Locate every blood parasite and identify its species.
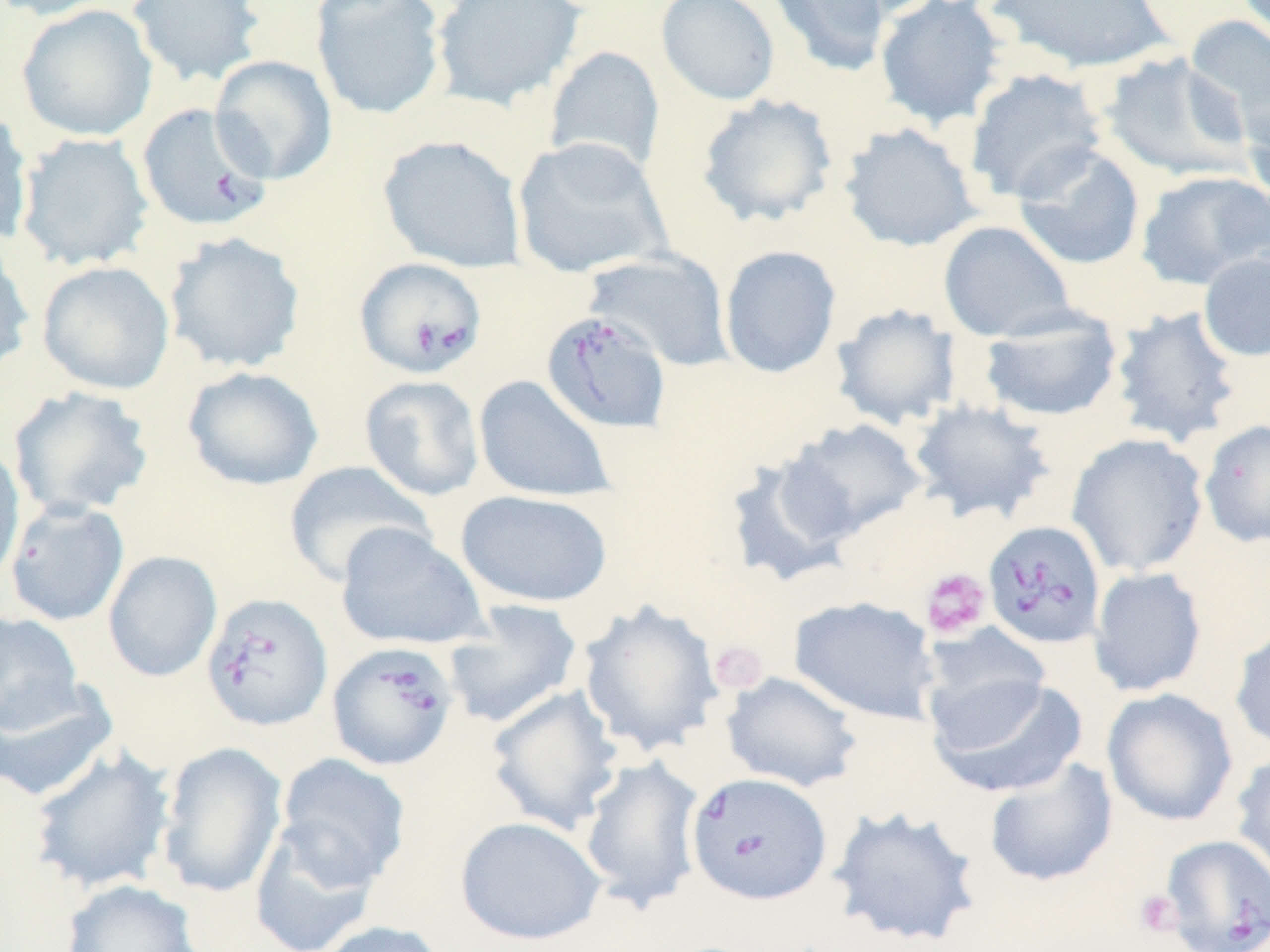

Approximate bounding boxes as named x1/y1/x2/y2 corners in pixels.
Babesia divergens-infected red blood cells: (x1=137, y1=102, x2=273, y2=232), (x1=354, y1=256, x2=488, y2=380), (x1=541, y1=310, x2=673, y2=435), (x1=983, y1=520, x2=1106, y2=649), (x1=199, y1=592, x2=333, y2=732), (x1=326, y1=640, x2=459, y2=771), (x1=686, y1=772, x2=832, y2=905), (x1=1158, y1=834, x2=1270, y2=951).
No Plasmodium falciparum, Plasmodium ovale, Plasmodium malariae, Plasmodium vivax, or Trypanosoma brucei observed.

Platelet locations: (x1=920, y1=567, x2=991, y2=640), (x1=709, y1=640, x2=769, y2=694), (x1=1134, y1=889, x2=1183, y2=937). Uninfected red blood cell locations: (x1=0, y1=0, x2=117, y2=20), (x1=126, y1=0, x2=265, y2=87), (x1=310, y1=0, x2=447, y2=120), (x1=431, y1=0, x2=586, y2=111), (x1=655, y1=0, x2=781, y2=106), (x1=766, y1=0, x2=892, y2=78), (x1=819, y1=0, x2=945, y2=20), (x1=875, y1=0, x2=1009, y2=130), (x1=989, y1=0, x2=1172, y2=73), (x1=16, y1=4, x2=158, y2=141), (x1=1184, y1=15, x2=1270, y2=147), (x1=544, y1=45, x2=666, y2=177), (x1=1099, y1=51, x2=1254, y2=183), (x1=209, y1=55, x2=338, y2=185), (x1=964, y1=68, x2=1109, y2=205), (x1=695, y1=93, x2=839, y2=228), (x1=1240, y1=93, x2=1270, y2=212), (x1=0, y1=107, x2=34, y2=247), (x1=838, y1=122, x2=983, y2=252), (x1=15, y1=132, x2=154, y2=271), (x1=378, y1=135, x2=527, y2=273), (x1=511, y1=136, x2=672, y2=279), (x1=1011, y1=144, x2=1146, y2=270), (x1=1134, y1=170, x2=1269, y2=290), (x1=938, y1=220, x2=1077, y2=342), (x1=163, y1=231, x2=307, y2=374), (x1=0, y1=236, x2=35, y2=377), (x1=719, y1=245, x2=842, y2=378), (x1=584, y1=249, x2=734, y2=370), (x1=1198, y1=251, x2=1270, y2=362), (x1=36, y1=260, x2=175, y2=394), (x1=829, y1=303, x2=963, y2=430), (x1=1108, y1=305, x2=1243, y2=449), (x1=978, y1=308, x2=1124, y2=423), (x1=182, y1=366, x2=324, y2=491), (x1=359, y1=374, x2=485, y2=502), (x1=473, y1=375, x2=616, y2=503), (x1=7, y1=385, x2=155, y2=520), (x1=907, y1=398, x2=1056, y2=526), (x1=781, y1=418, x2=928, y2=541), (x1=1199, y1=418, x2=1270, y2=548), (x1=1066, y1=432, x2=1209, y2=577), (x1=0, y1=441, x2=25, y2=587), (x1=723, y1=452, x2=860, y2=586), (x1=283, y1=461, x2=435, y2=587), (x1=455, y1=489, x2=614, y2=608), (x1=4, y1=500, x2=130, y2=626), (x1=335, y1=522, x2=488, y2=651), (x1=102, y1=550, x2=222, y2=682), (x1=1088, y1=567, x2=1207, y2=697), (x1=789, y1=595, x2=939, y2=725), (x1=443, y1=599, x2=583, y2=730), (x1=576, y1=599, x2=726, y2=757), (x1=0, y1=611, x2=85, y2=734), (x1=921, y1=624, x2=1052, y2=736), (x1=1229, y1=624, x2=1270, y2=754), (x1=720, y1=671, x2=863, y2=792), (x1=927, y1=674, x2=1088, y2=798), (x1=0, y1=679, x2=118, y2=803), (x1=485, y1=684, x2=625, y2=836), (x1=1101, y1=687, x2=1238, y2=827), (x1=156, y1=741, x2=288, y2=898), (x1=29, y1=746, x2=177, y2=895), (x1=1230, y1=751, x2=1270, y2=883), (x1=276, y1=752, x2=411, y2=889), (x1=578, y1=754, x2=706, y2=913), (x1=983, y1=757, x2=1118, y2=887), (x1=826, y1=804, x2=983, y2=950), (x1=455, y1=815, x2=606, y2=947), (x1=248, y1=820, x2=383, y2=952), (x1=60, y1=879, x2=203, y2=952), (x1=313, y1=919, x2=450, y2=952). Slide-level diagnosis: Babesia divergens. One field of a larger specimen. Image is 1270×952 pixels. May-Grünwald-Giemsa stain. Light microscopy. Captured at 1000x magnification. Thin blood smear.